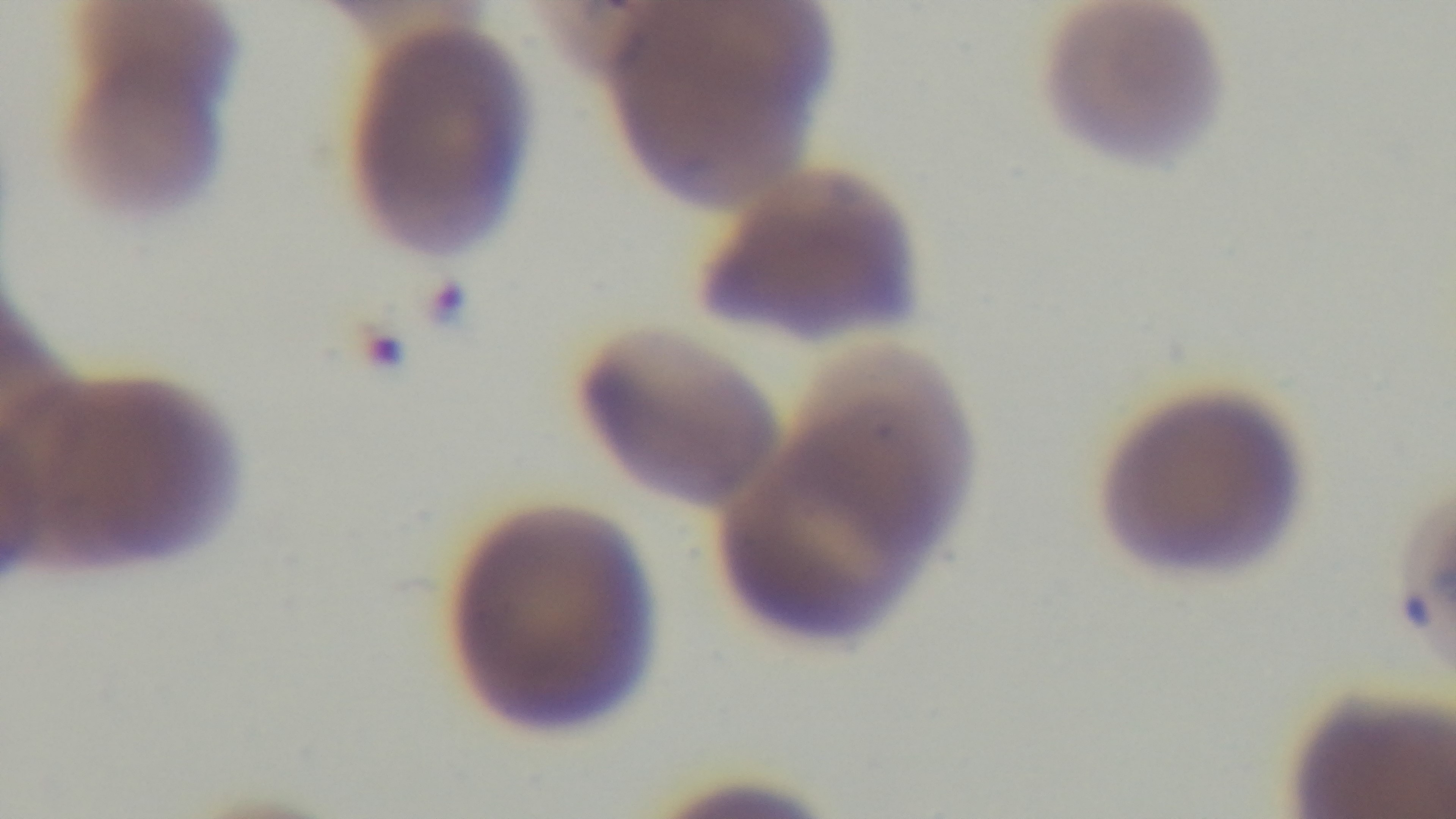
Summary:
  - Field of view: one from the slide
  - Stain: Giemsa
  - Modality: light microscopy
  - Objective: 100x oil immersion
  - Capture: mounted 4K digital camera
  - Preparation: thin blood film
  - Malaria status: infected